Outline each blood parasite and name the species.
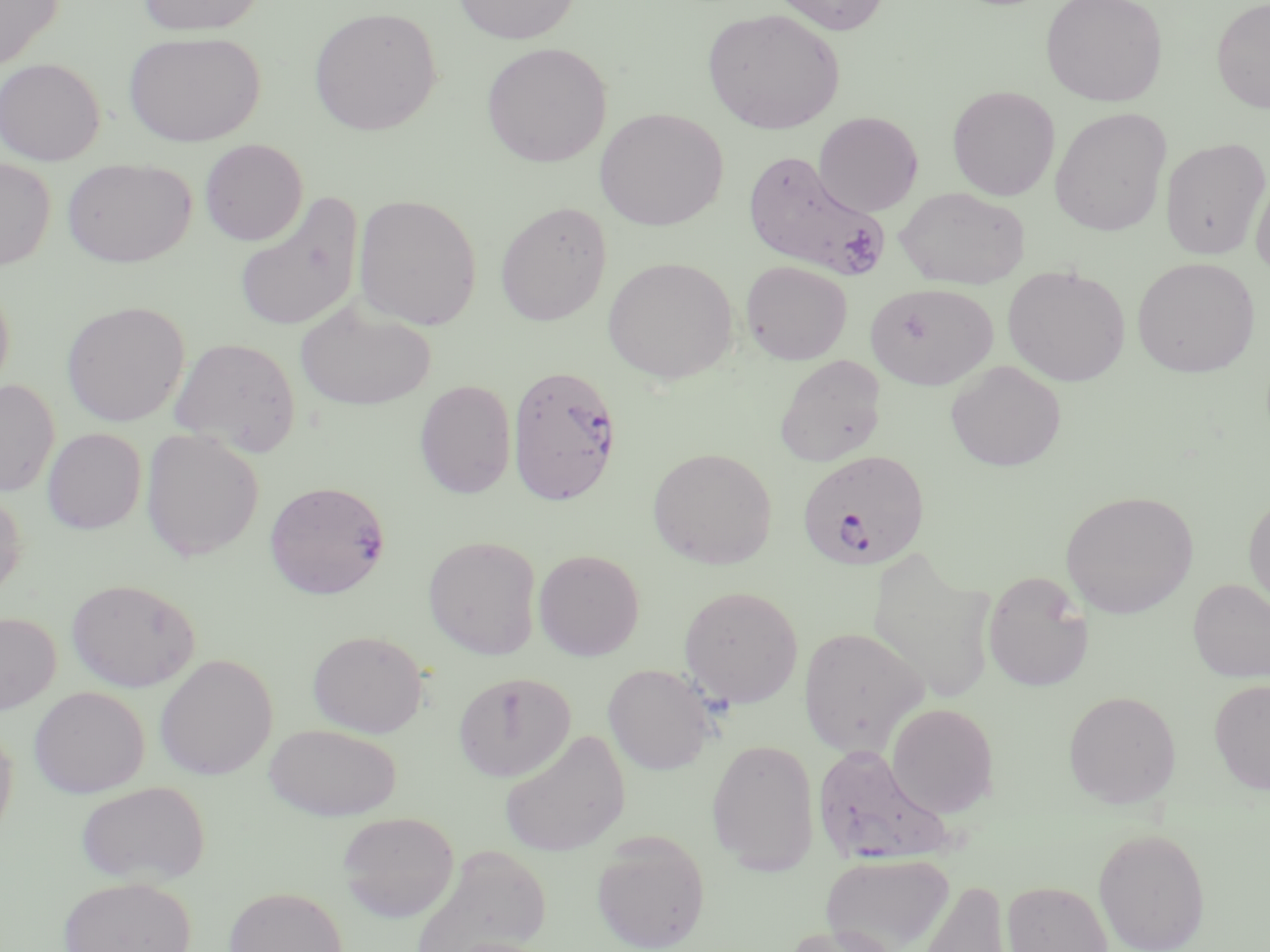

Approximate bounding boxes as [x1, y1, x2, y2] in pixels.
Plasmodium falciparum-infected red blood cells: [742, 150, 891, 281], [507, 364, 622, 506], [797, 449, 930, 572].
No Plasmodium ovale, Plasmodium malariae, Plasmodium vivax, Babesia divergens, or Trypanosoma brucei observed.

Uninfected red blood cell locations: [0, 0, 64, 72], [136, 0, 267, 36], [452, 0, 581, 44], [769, 0, 892, 35], [1040, 0, 1169, 107], [1211, 0, 1270, 114], [309, 7, 442, 136], [702, 8, 844, 134], [123, 31, 266, 147], [481, 41, 612, 168], [0, 58, 105, 166], [947, 85, 1059, 201], [1050, 107, 1171, 236], [594, 108, 729, 231], [813, 111, 924, 216], [1161, 137, 1269, 260], [199, 139, 308, 246], [0, 156, 55, 271], [62, 157, 196, 267], [1250, 170, 1270, 279], [895, 187, 1030, 289], [233, 191, 364, 334], [352, 194, 483, 330], [495, 201, 612, 326], [603, 256, 738, 385], [1131, 256, 1261, 377], [740, 260, 853, 365], [1002, 265, 1131, 386], [0, 275, 14, 398], [865, 283, 997, 389], [62, 301, 190, 426], [295, 302, 436, 411], [169, 337, 302, 456], [773, 354, 886, 467], [945, 361, 1067, 472], [0, 379, 60, 497], [414, 380, 517, 499], [140, 427, 264, 561], [43, 428, 146, 535], [647, 447, 777, 569], [265, 480, 391, 599], [0, 489, 26, 601], [1060, 490, 1198, 619], [1243, 491, 1270, 616], [423, 535, 541, 660], [866, 546, 997, 705], [533, 549, 645, 661], [982, 571, 1094, 692], [66, 578, 201, 692], [1188, 578, 1270, 682], [679, 585, 803, 708], [0, 611, 61, 714], [798, 627, 928, 756], [308, 630, 428, 737], [155, 653, 277, 780], [603, 663, 715, 774], [453, 671, 576, 782], [1209, 678, 1270, 795], [29, 686, 149, 798], [1063, 690, 1181, 808], [887, 703, 999, 818], [0, 720, 18, 844], [264, 723, 402, 820], [499, 730, 631, 856], [706, 738, 819, 874], [813, 743, 953, 866], [75, 780, 210, 886], [337, 811, 459, 922], [1093, 826, 1211, 952], [590, 832, 711, 952], [409, 845, 551, 952], [821, 853, 954, 952], [58, 876, 198, 952], [917, 878, 1013, 952], [1001, 881, 1113, 952], [224, 886, 347, 952], [780, 922, 902, 952]. Slide-level diagnosis: Plasmodium falciparum. Thin blood film. May-Grünwald-Giemsa stain. Image is 1270×952 pixels. Optical microscopy. Captured at 1000x magnification. One field of a larger specimen.